Identify the blood parasite species.
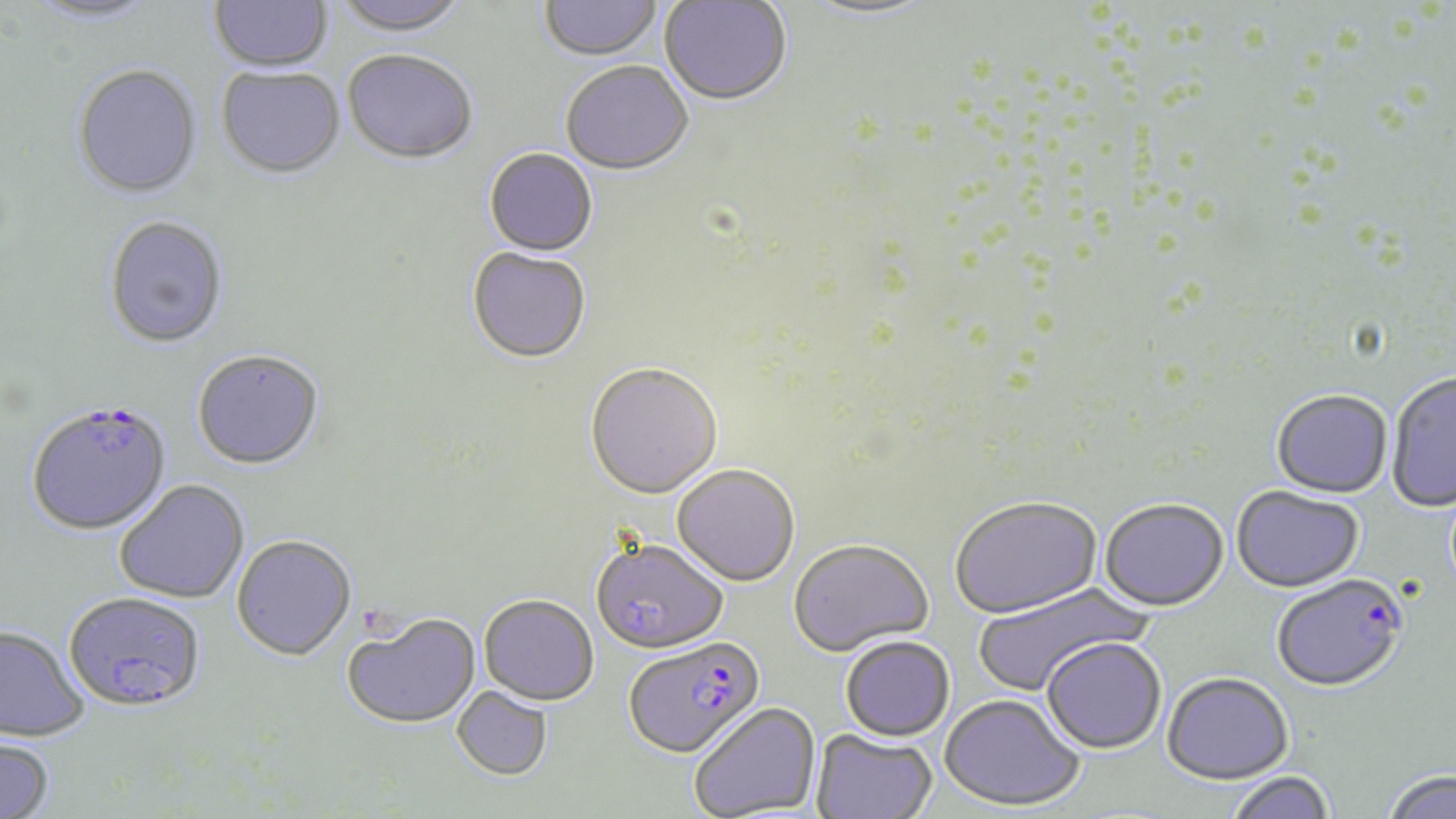
Plasmodium falciparum.

Summary:
  - Coordinate format: approximate bounding boxes as named x1/y1/x2/y2 corners in pixels
  - Uninfected red blood cell locations: (x1=208, y1=0, x2=333, y2=75), (x1=331, y1=0, x2=470, y2=39), (x1=24, y1=1, x2=162, y2=28), (x1=539, y1=1, x2=663, y2=64), (x1=659, y1=1, x2=792, y2=108), (x1=801, y1=1, x2=937, y2=22), (x1=342, y1=53, x2=477, y2=167), (x1=561, y1=63, x2=693, y2=177), (x1=72, y1=66, x2=203, y2=202), (x1=216, y1=69, x2=345, y2=182), (x1=483, y1=150, x2=598, y2=258), (x1=103, y1=217, x2=229, y2=349), (x1=466, y1=249, x2=591, y2=365), (x1=191, y1=351, x2=325, y2=472), (x1=585, y1=364, x2=723, y2=500), (x1=1386, y1=372, x2=1456, y2=512), (x1=1271, y1=390, x2=1392, y2=499), (x1=672, y1=464, x2=800, y2=586), (x1=114, y1=479, x2=249, y2=603), (x1=1232, y1=487, x2=1365, y2=593), (x1=950, y1=497, x2=1103, y2=621), (x1=1098, y1=500, x2=1229, y2=614), (x1=231, y1=535, x2=356, y2=661), (x1=591, y1=537, x2=728, y2=654), (x1=788, y1=540, x2=934, y2=658), (x1=972, y1=582, x2=1152, y2=696), (x1=479, y1=594, x2=599, y2=706), (x1=342, y1=613, x2=481, y2=729), (x1=0, y1=625, x2=88, y2=741), (x1=841, y1=636, x2=955, y2=742), (x1=1042, y1=638, x2=1166, y2=755), (x1=1162, y1=673, x2=1294, y2=785), (x1=452, y1=686, x2=553, y2=780), (x1=939, y1=694, x2=1086, y2=813), (x1=690, y1=702, x2=821, y2=818), (x1=811, y1=729, x2=938, y2=819), (x1=0, y1=736, x2=55, y2=819), (x1=1381, y1=770, x2=1456, y2=819), (x1=1225, y1=772, x2=1337, y2=819)
  - Plasmodium falciparum-infected red blood cell locations: (x1=26, y1=400, x2=172, y2=536), (x1=1271, y1=575, x2=1408, y2=694), (x1=63, y1=590, x2=206, y2=711), (x1=623, y1=636, x2=765, y2=758)
  - Field of view: single
  - Modality: optical microscopy
  - Stain: May-Grünwald-Giemsa
  - Preparation: thin blood film
  - Magnification: 1000x
  - Image size: 1456×819 pixels